Report the malaria status of this cell.
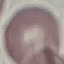

It is uninfected.

stain = Giemsa
image type = cell patch, automatically extracted from a larger field of view and resized to 64 × 64 pixels
preparation = thin blood film
capture = smartphone through the microscope eyepiece